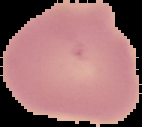
result = no Plasmodium parasites seen
image type = cell region segmented out of the field of view; surrounding area masked to black
image size = 142×127 pixels
preparation = thin blood smear